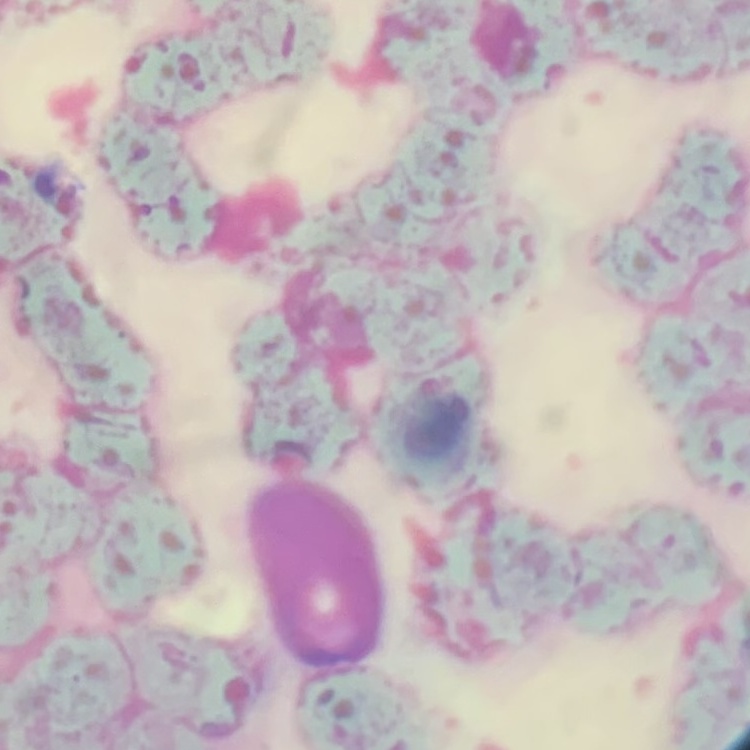 The red blood cells exhibit rouleaux formation. Thin blood smear. Square crop of a larger photomicrograph. Field's or Giemsa stain.